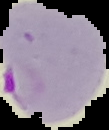

preparation: thin blood smear
image_size: 109×130 pixels
result: malaria parasites detected
image_type: cell region segmented out of the field of view; surrounding area masked to black